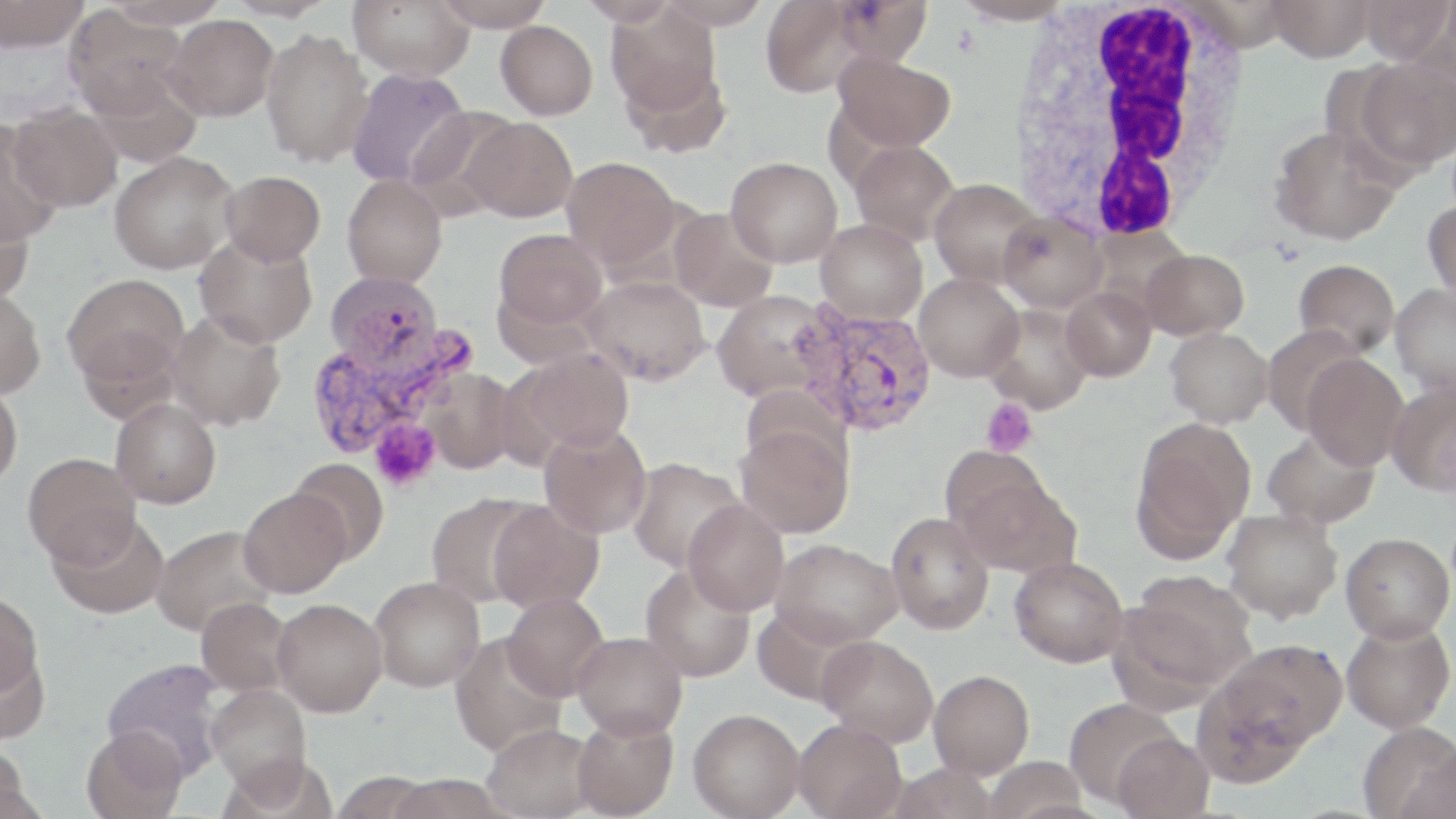
Approximate bounding boxes as [x1, y1, x2, y2] in pixels. White blood cell locations: [1007, 0, 1255, 240]. Uninfected red blood cell locations: [0, 0, 89, 52], [105, 0, 230, 28], [221, 0, 338, 21], [349, 0, 475, 81], [431, 0, 556, 32], [577, 0, 680, 25], [830, 0, 934, 66], [1266, 0, 1376, 61], [1356, 0, 1454, 65], [657, 1, 771, 29], [760, 1, 868, 98], [951, 1, 1076, 26], [606, 2, 725, 129], [64, 6, 189, 120], [163, 14, 278, 121], [496, 20, 598, 119], [260, 29, 373, 168], [833, 52, 956, 152], [1351, 56, 1456, 173], [346, 68, 471, 189], [6, 104, 124, 212], [407, 105, 521, 218], [461, 117, 577, 222], [0, 120, 65, 245], [1268, 124, 1402, 245], [850, 139, 959, 244], [109, 151, 239, 274], [726, 156, 842, 267], [561, 158, 682, 271], [220, 170, 325, 265], [342, 175, 447, 288], [929, 177, 1043, 287], [0, 195, 35, 306], [1422, 199, 1456, 301], [669, 207, 778, 312], [998, 211, 1107, 312], [816, 219, 927, 324], [493, 228, 608, 334], [194, 233, 317, 348], [1142, 248, 1249, 340], [1294, 259, 1400, 357], [324, 270, 447, 374], [62, 273, 189, 392], [914, 273, 1024, 382], [581, 275, 710, 386], [1390, 283, 1456, 397], [1062, 286, 1157, 382], [0, 287, 46, 400], [712, 290, 832, 403], [982, 303, 1093, 414], [166, 311, 287, 431], [1261, 325, 1367, 434], [1165, 327, 1273, 428], [510, 348, 635, 455], [1303, 354, 1409, 470], [423, 369, 518, 474], [0, 380, 23, 492], [1386, 380, 1456, 497], [111, 398, 222, 509], [1131, 419, 1255, 559], [735, 422, 855, 539], [539, 423, 652, 539], [1262, 428, 1381, 528], [23, 453, 142, 567], [627, 457, 744, 571], [288, 458, 389, 565], [952, 466, 1081, 579], [238, 488, 350, 597], [426, 492, 538, 607], [488, 500, 604, 613], [683, 500, 790, 616], [1222, 509, 1343, 623], [886, 511, 995, 635], [48, 512, 170, 619], [151, 526, 278, 636], [1340, 532, 1454, 642], [771, 539, 903, 647], [1010, 556, 1128, 667], [639, 562, 757, 682], [1119, 573, 1257, 697], [371, 576, 484, 691], [0, 591, 43, 700], [502, 592, 609, 701], [195, 597, 294, 698], [272, 598, 387, 716], [1341, 619, 1455, 733], [572, 631, 687, 740], [449, 634, 567, 757], [817, 635, 939, 747], [1214, 638, 1348, 753], [0, 644, 50, 745], [102, 657, 227, 778], [929, 670, 1035, 779], [207, 685, 311, 796], [1062, 698, 1182, 808], [688, 708, 805, 818], [572, 714, 679, 819], [793, 718, 906, 819], [1358, 721, 1456, 818], [483, 723, 598, 818], [81, 726, 187, 819], [1111, 731, 1216, 819], [1398, 745, 1456, 819], [0, 746, 31, 817], [981, 756, 1091, 819], [329, 772, 436, 818], [383, 774, 512, 819]. Plasmodium vivax-infected red blood cell locations: [791, 302, 937, 436], [302, 322, 480, 461]. Platelet locations: [981, 398, 1037, 457], [369, 418, 442, 491]. Slide-level diagnosis: Plasmodium vivax. 1000x magnification. Thin blood film. One field of a larger specimen. May-Grünwald-Giemsa stain. Image is 1456×819 pixels. Optical microscopy.